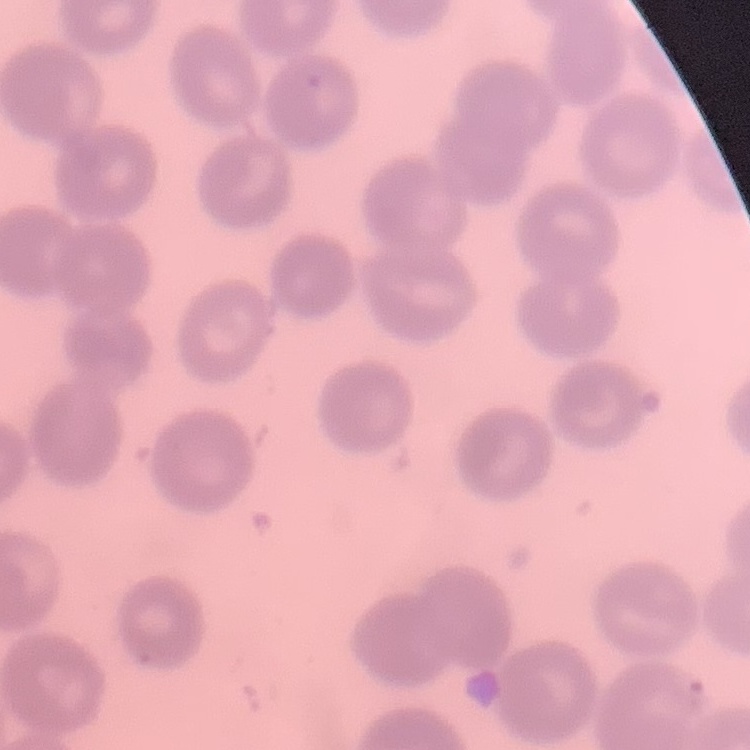

Summary:
  - Erythrocyte morphology: no rouleaux formation
  - Image type: square crop of a larger photomicrograph
  - Preparation: thin peripheral smear
  - Stain: Field's or Giemsa